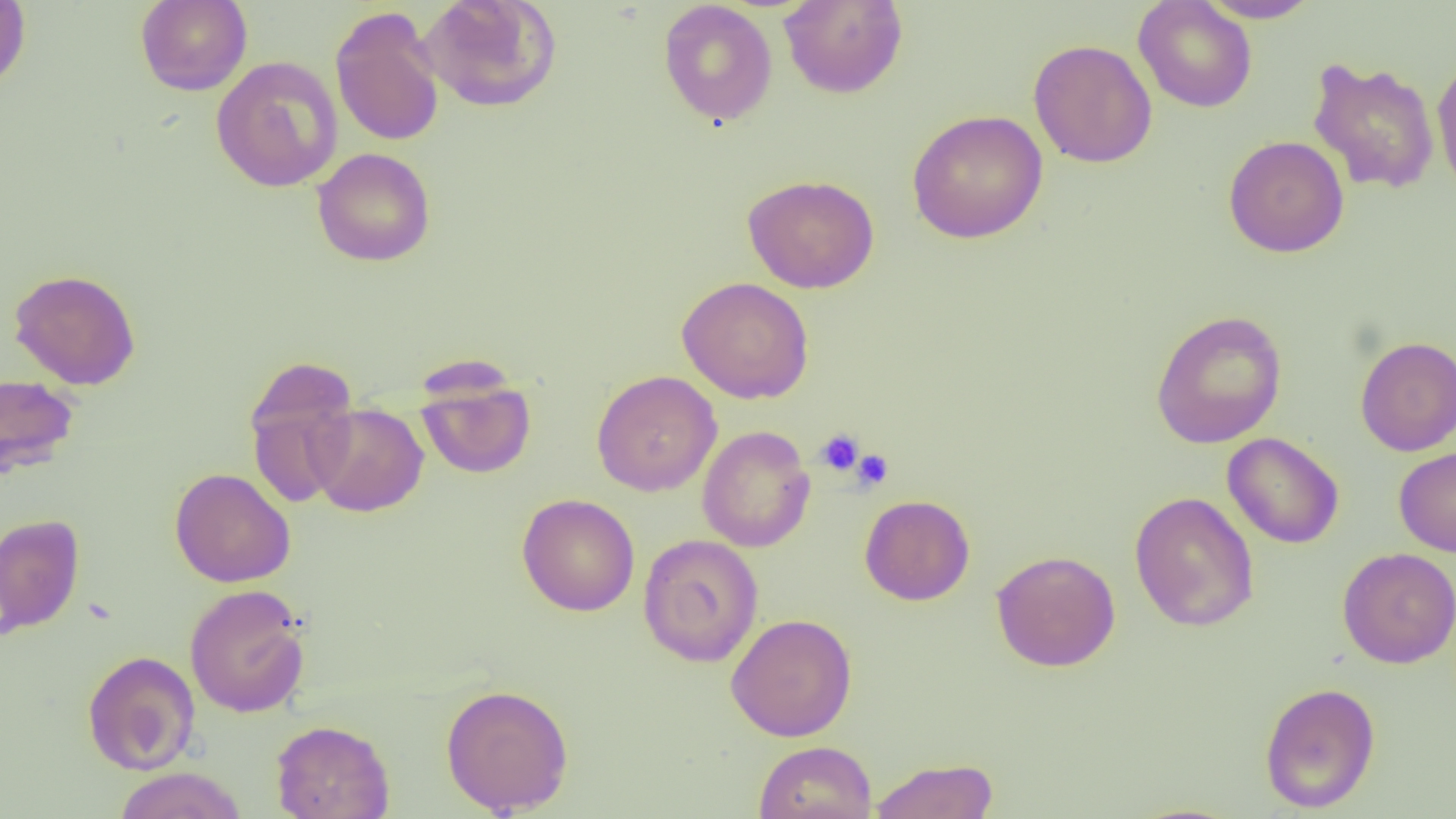
Summary:
  - Coordinate format: approximate bounding boxes as named x1/y1/x2/y2 corners in pixels
  - Uninfected red blood cell locations: (x1=0, y1=0, x2=31, y2=91), (x1=136, y1=0, x2=252, y2=96), (x1=419, y1=0, x2=561, y2=114), (x1=779, y1=0, x2=908, y2=99), (x1=1197, y1=0, x2=1323, y2=23), (x1=658, y1=1, x2=778, y2=126), (x1=1133, y1=1, x2=1257, y2=113), (x1=330, y1=6, x2=445, y2=148), (x1=1028, y1=39, x2=1157, y2=168), (x1=1432, y1=54, x2=1456, y2=201), (x1=210, y1=56, x2=343, y2=192), (x1=1307, y1=57, x2=1440, y2=195), (x1=907, y1=110, x2=1048, y2=243), (x1=1223, y1=135, x2=1349, y2=258), (x1=312, y1=147, x2=436, y2=266), (x1=741, y1=174, x2=880, y2=294), (x1=9, y1=268, x2=141, y2=390), (x1=676, y1=276, x2=814, y2=403), (x1=1150, y1=309, x2=1288, y2=449), (x1=1355, y1=336, x2=1456, y2=456), (x1=243, y1=362, x2=360, y2=508), (x1=592, y1=370, x2=722, y2=496), (x1=0, y1=372, x2=80, y2=478), (x1=416, y1=374, x2=536, y2=479), (x1=310, y1=403, x2=429, y2=517), (x1=697, y1=425, x2=815, y2=553), (x1=1222, y1=432, x2=1344, y2=549), (x1=1394, y1=446, x2=1456, y2=557), (x1=169, y1=468, x2=296, y2=588), (x1=1129, y1=491, x2=1260, y2=632), (x1=516, y1=493, x2=640, y2=617), (x1=860, y1=494, x2=975, y2=606), (x1=0, y1=513, x2=85, y2=637), (x1=638, y1=534, x2=764, y2=667), (x1=1338, y1=547, x2=1456, y2=669), (x1=991, y1=550, x2=1121, y2=672), (x1=184, y1=584, x2=310, y2=718), (x1=726, y1=613, x2=857, y2=741), (x1=82, y1=650, x2=200, y2=775), (x1=1259, y1=681, x2=1381, y2=814), (x1=440, y1=683, x2=574, y2=816), (x1=270, y1=719, x2=395, y2=819), (x1=753, y1=740, x2=877, y2=819), (x1=869, y1=757, x2=1000, y2=819), (x1=113, y1=767, x2=247, y2=819)
  - Platelet locations: (x1=815, y1=428, x2=864, y2=476), (x1=851, y1=450, x2=893, y2=490)
  - Slide-level diagnosis: negative for blood parasites
  - Image size: 1456×819 pixels
  - Preparation: thin blood smear
  - Modality: light microscopy
  - Magnification: 1000x
  - Field of view: single